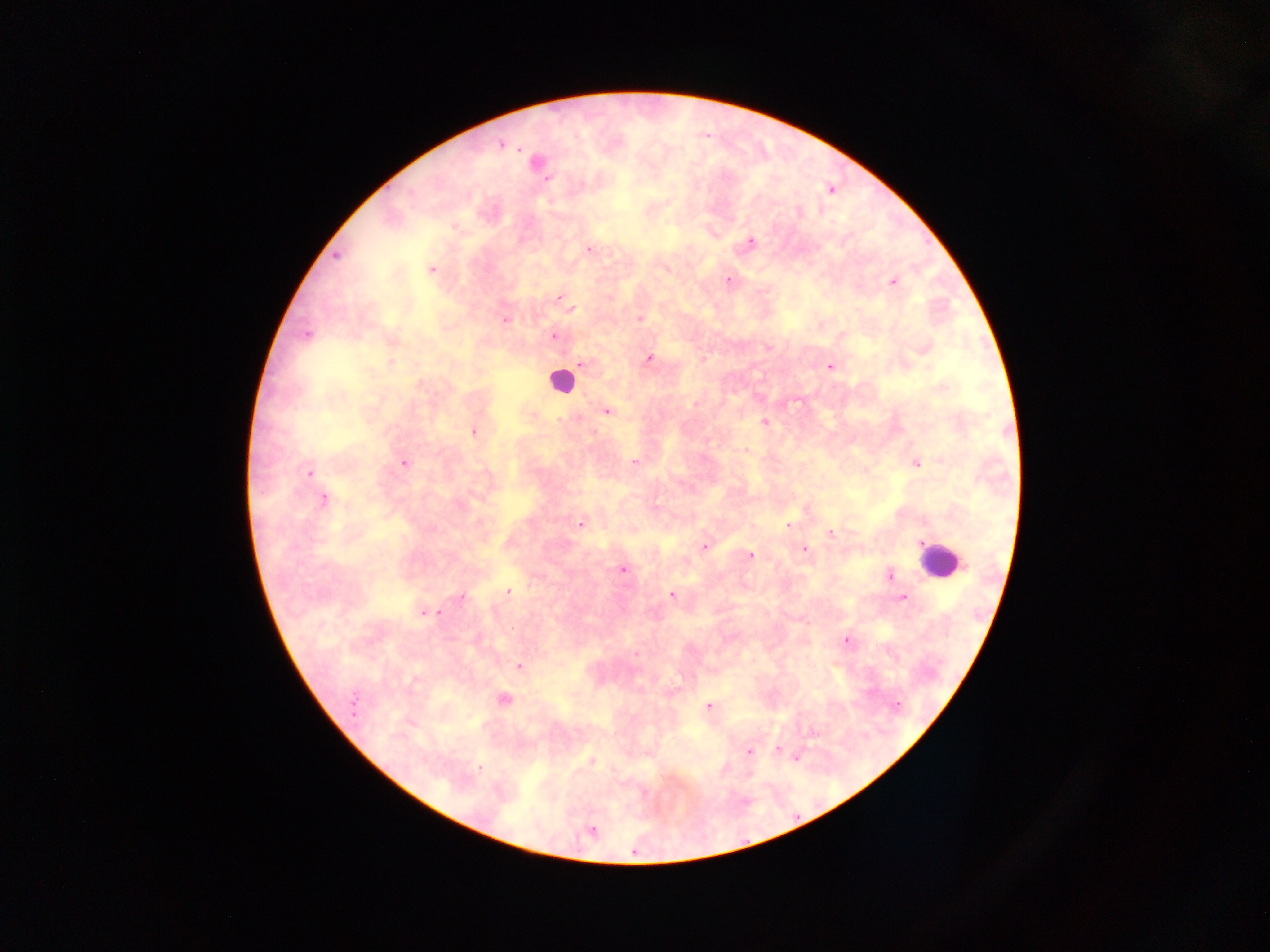
Approximate centers as x y in pixels.
Summary:
  - Malaria parasite locations: 501 144; 535 163; 829 189; 454 226; 750 242; 589 249; 335 255; 430 269; 728 280; 892 282; 560 297; 570 309; 639 318; 504 320; 305 335; 553 336; 390 340; 923 348; 649 359; 391 362; 581 363; 830 366; 606 411; 531 414; 764 422; 473 431; 747 451; 634 461; 915 462; 403 463; 308 472; 322 499; 581 522; 790 524; 830 533; 704 546; 803 549; 750 555; 622 569; 890 574; 508 592; 671 595; 461 597; 902 597; 425 613; 845 640; 635 653; 519 666; 504 700; 708 707; 813 732; 749 750; 778 751; 795 756; 591 760; 590 830
  - Leukocyte locations: 559 381; 941 561
  - Field of view: single
  - Image size: 1270×952 pixels
  - Capture: mobile-phone photograph through a microscope
  - Country: Ghana
  - Preparation: thick blood smear